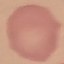

Summary:
  - Malaria status: uninfected
  - Stain: Giemsa
  - Preparation: thin smear
  - Capture: smartphone through the microscope eyepiece
  - Image type: automatically extracted cell patch, resized to 64 × 64 pixels